Classify this cell by malaria status.
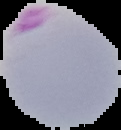
It is parasitized.

Summary:
  - Image type: cell region segmented out of the field of view; surrounding area masked to black
  - Preparation: thin blood smear
  - Image size: 121×130 pixels